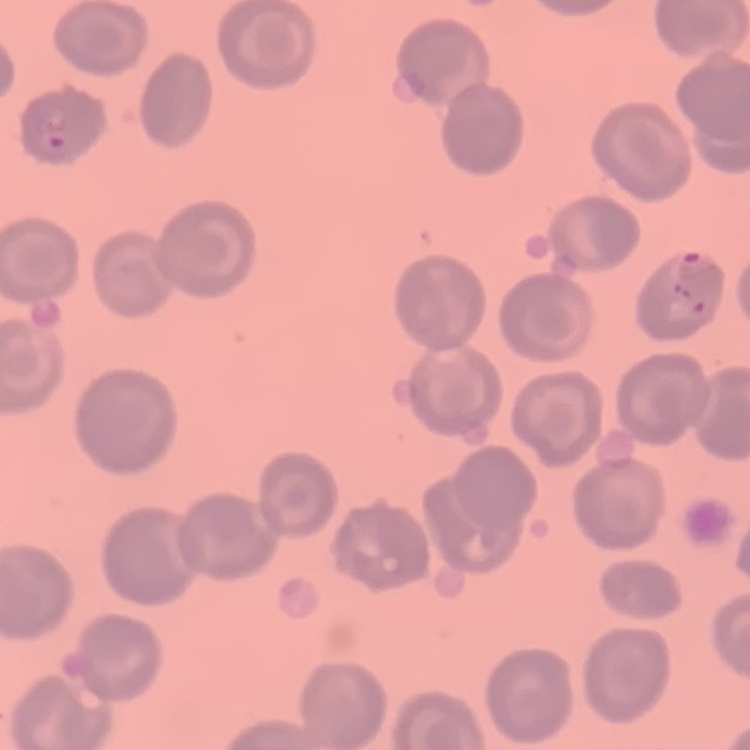

The red blood cells exhibit no rouleaux formation. Square crop of a larger photomicrograph. Thin blood film. Stained with either Field's or Giemsa.